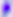

Summary:
  - Modality: micrograph
  - Magnification: 400x
  - Identification: Toxoplasma gondii